Classify this cell by malaria status.
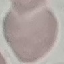

It is uninfected.

Summary:
  - Preparation: thin smear
  - Stain: Giemsa
  - Image type: cell patch, automatically extracted from a larger field of view and resized to 64 × 64 pixels
  - Capture: smartphone camera at the microscope eyepiece